Classify this cell by malaria status.
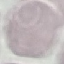
Uninfected.

preparation: thin blood smear
capture: smartphone camera at the microscope eyepiece
stain: Giemsa
image_type: automatically extracted cell patch, resized to 64 × 64 pixels